Outline each white blood cell.
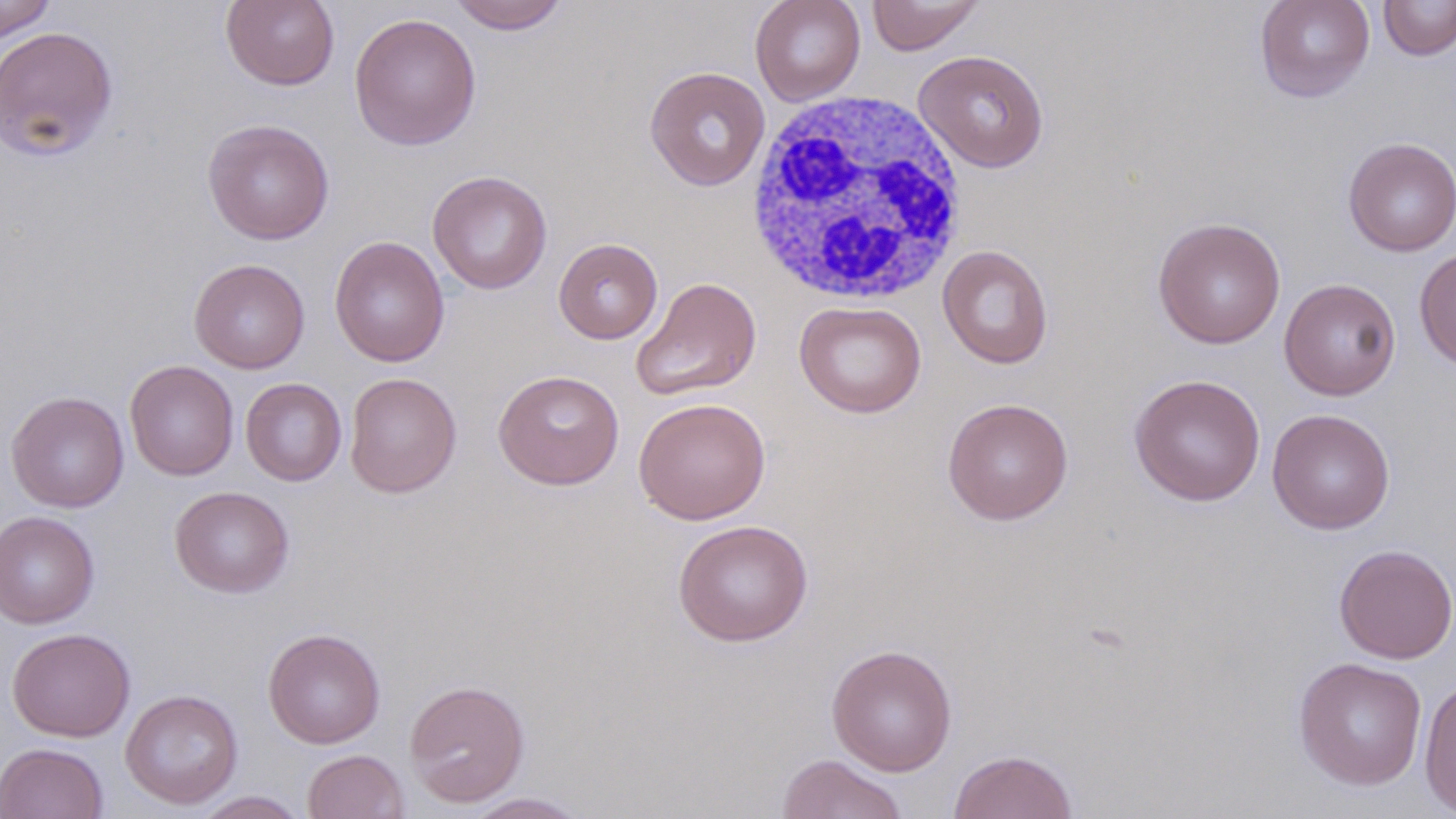

Approximate bounding boxes as (x1, y1, x2, y2) in pixels.
White blood cells: (744, 91, 969, 307).

slide-level diagnosis = no evidence of blood parasites
magnification = 1000x
uninfected red blood cell locations = approximate bounding boxes as (x1, y1, x2, y2) in pixels: (0, 0, 56, 41), (221, 0, 340, 91), (750, 0, 866, 106), (866, 0, 985, 55), (1254, 0, 1375, 103), (1378, 0, 1456, 60), (448, 1, 570, 34), (349, 12, 482, 150), (0, 25, 119, 162), (913, 49, 1050, 173), (644, 66, 771, 191), (202, 118, 335, 244), (1342, 137, 1456, 257), (427, 169, 552, 294), (1152, 216, 1286, 349), (329, 236, 450, 368), (553, 238, 663, 344), (937, 244, 1054, 369), (1414, 247, 1456, 373), (188, 258, 310, 374), (631, 276, 762, 402), (1278, 278, 1401, 400), (794, 301, 926, 418), (125, 360, 239, 480), (493, 369, 625, 490), (344, 372, 462, 498), (1129, 373, 1267, 507), (241, 378, 347, 486), (5, 391, 129, 513), (632, 397, 771, 524), (942, 397, 1074, 525), (1267, 408, 1395, 535), (169, 485, 294, 598), (0, 511, 100, 629), (673, 519, 814, 646), (1333, 543, 1456, 665), (6, 627, 136, 742), (263, 628, 385, 749), (826, 644, 958, 776), (1292, 657, 1428, 791), (1418, 676, 1456, 815), (404, 679, 530, 807), (120, 689, 243, 809), (0, 742, 108, 819), (303, 749, 409, 819), (949, 749, 1078, 819), (776, 754, 909, 819), (192, 790, 310, 818), (462, 792, 591, 818)
stain = May-Grünwald-Giemsa
preparation = thin blood smear
modality = light microscopy
field of view = one of a larger specimen
image size = 1456×819 pixels